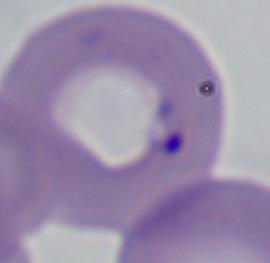

A Babesia parasite is seen. 1000x magnification. Micrograph.